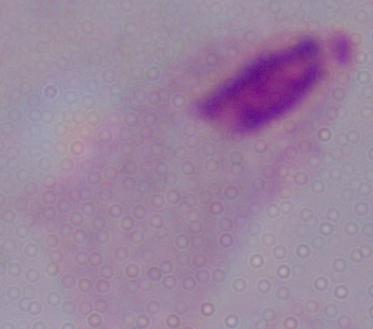 A trichomonad is seen. Photomicrograph. Captured at 1000x magnification.